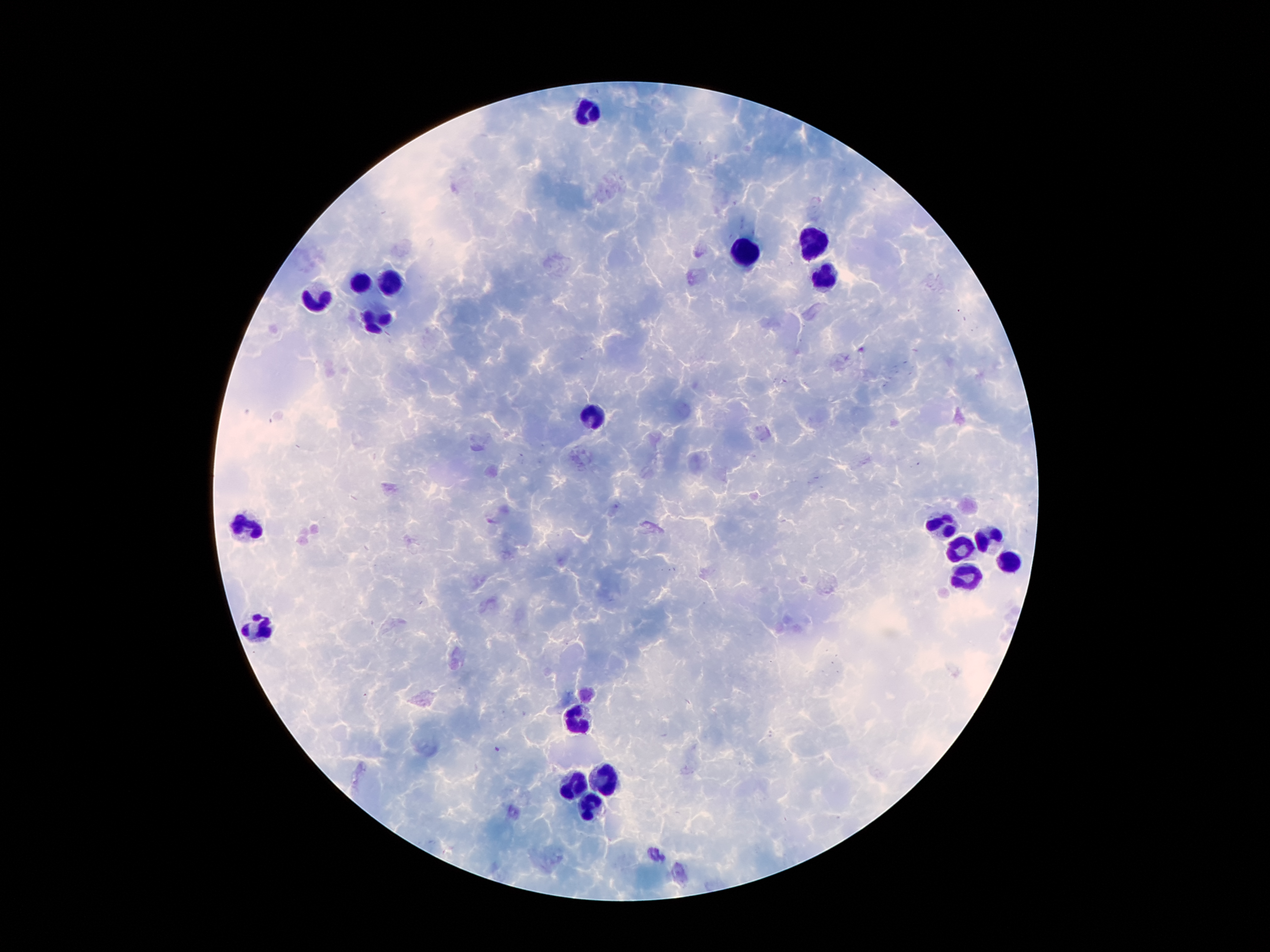

Approximate object centers, in pixels from the top-left corner.
Summary:
  - Leukocyte locations: (x=587, y=115), (x=808, y=241), (x=745, y=254), (x=822, y=275), (x=390, y=281), (x=358, y=283), (x=321, y=298), (x=377, y=321), (x=594, y=417), (x=249, y=525), (x=938, y=529), (x=990, y=541), (x=959, y=548), (x=1011, y=562), (x=965, y=577), (x=258, y=626), (x=571, y=720), (x=606, y=777), (x=575, y=787), (x=591, y=808)
  - Malaria parasite locations: (x=497, y=750)
  - Stain: Giemsa
  - Magnification: 100x
  - Image size: 1270×952 pixels
  - Preparation: thick peripheral-blood smear
  - Patient malaria status: infected with Plasmodium falciparum
  - Field of view: one from this slide
  - Capture: smartphone camera through the microscope eyepiece